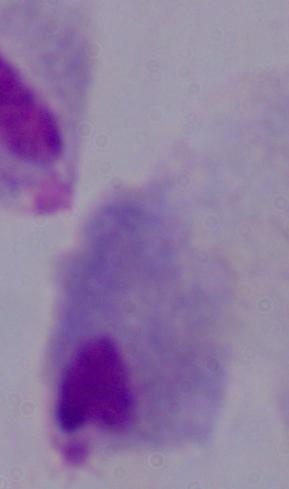
Summary:
  - Magnification: 1000x
  - Identification: trichomonad
  - Modality: micrograph